State which parasite is depicted.
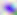
This is Toxoplasma gondii.

Summary:
  - Magnification: 400x
  - Modality: micrograph